Point out each malaria parasite.
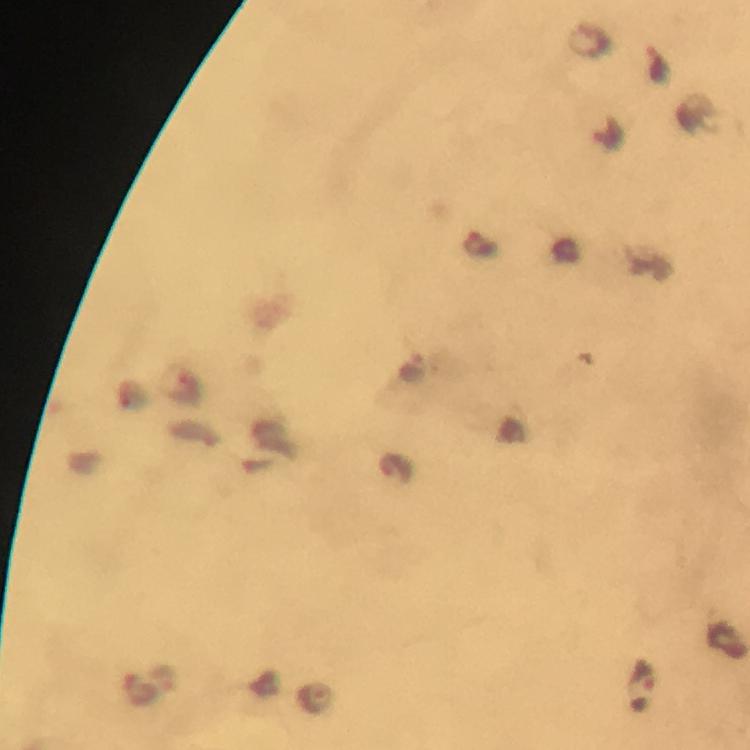
Approximate centers as {x, y} in pixels.
Malaria parasites: {659, 61}, {478, 243}, {413, 366}, {183, 385}, {395, 468}, {643, 676}, {164, 678}, {317, 697}.

cropped from = one field of view
image size = 750×750 pixels
context = from a diagnostic examination for malaria
preparation = thick smear
immersion oil = used
magnification = 100x
capture = smartphone camera through the microscope
stain = Giemsa